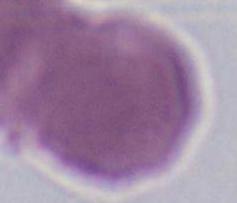

A red blood cell is seen. Micrograph. 1000x magnification.